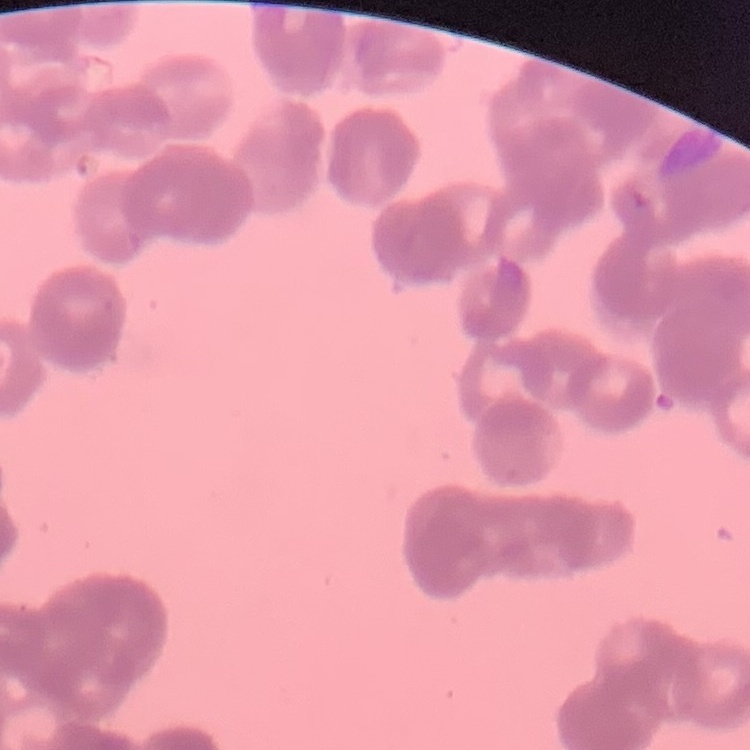

red blood cell morphology = rouleaux formation
preparation = thin peripheral smear
image type = one tile cut from a larger photomicrograph
stain = Field's or Giemsa